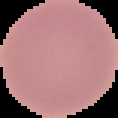
image size = 118×118 pixels
image type = cell region segmented out of the field of view; surrounding area masked to black
preparation = thin blood film
malaria status = uninfected